State which cell type is depicted.
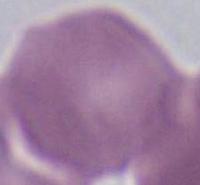
An erythrocyte.

Summary:
  - Magnification: 1000x
  - Modality: micrograph